Describe the morphology of the erythrocytes.
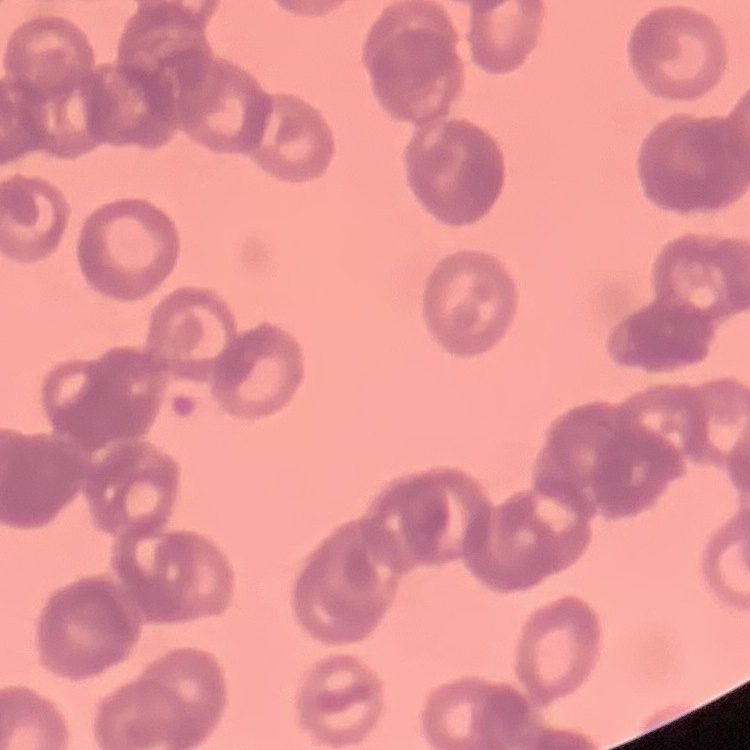

Rouleaux formation.

Square crop of a larger photomicrograph. Thin blood smear. Field's or Giemsa stain.